Name the parasite shown.
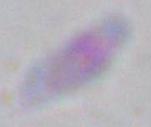
Toxoplasma gondii.

{
  "magnification": "1000x",
  "modality": "photomicrograph"
}